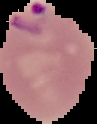

Summary:
  - Image type: segmented cell region with the area outside set to black
  - Result: malaria parasites detected
  - Preparation: thin blood film
  - Image size: 97×124 pixels